Identify the preparation type.
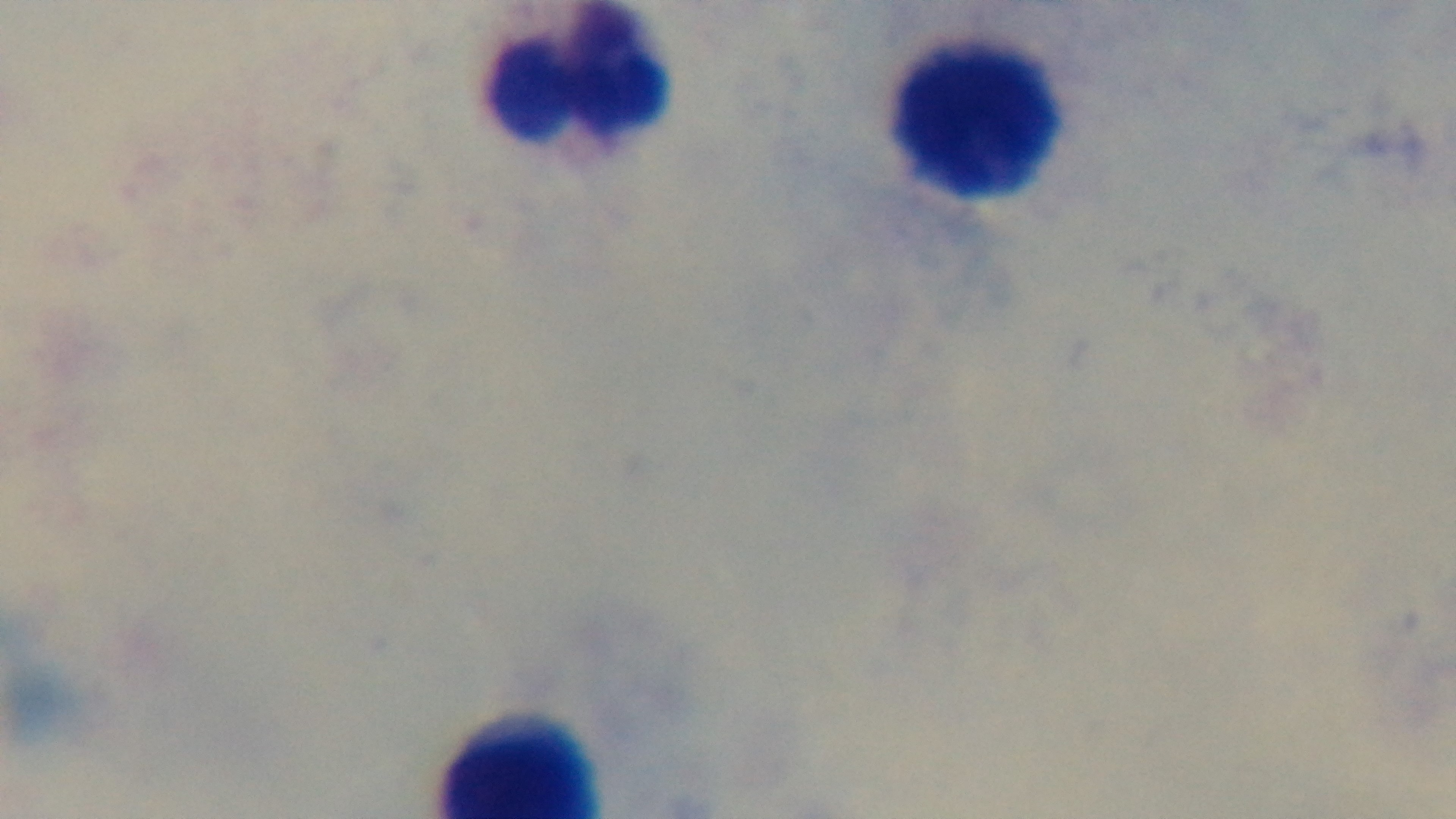

Thick.

Malaria status: uninfected. Photomicrograph. Giemsa-stained. Mounted 4K digital camera. One field from the slide. Oil-immersion objective, 100x.